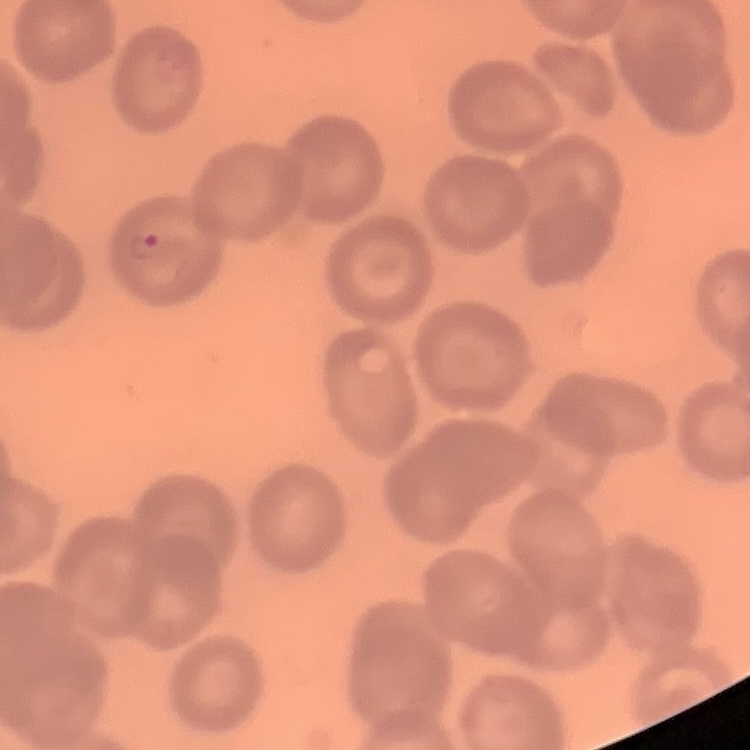
Summary:
  - Red blood cell morphology: no rouleaux formation
  - Image type: square crop of a larger photomicrograph
  - Stain: Field's or Giemsa
  - Preparation: thin blood smear